Name the blood parasite species.
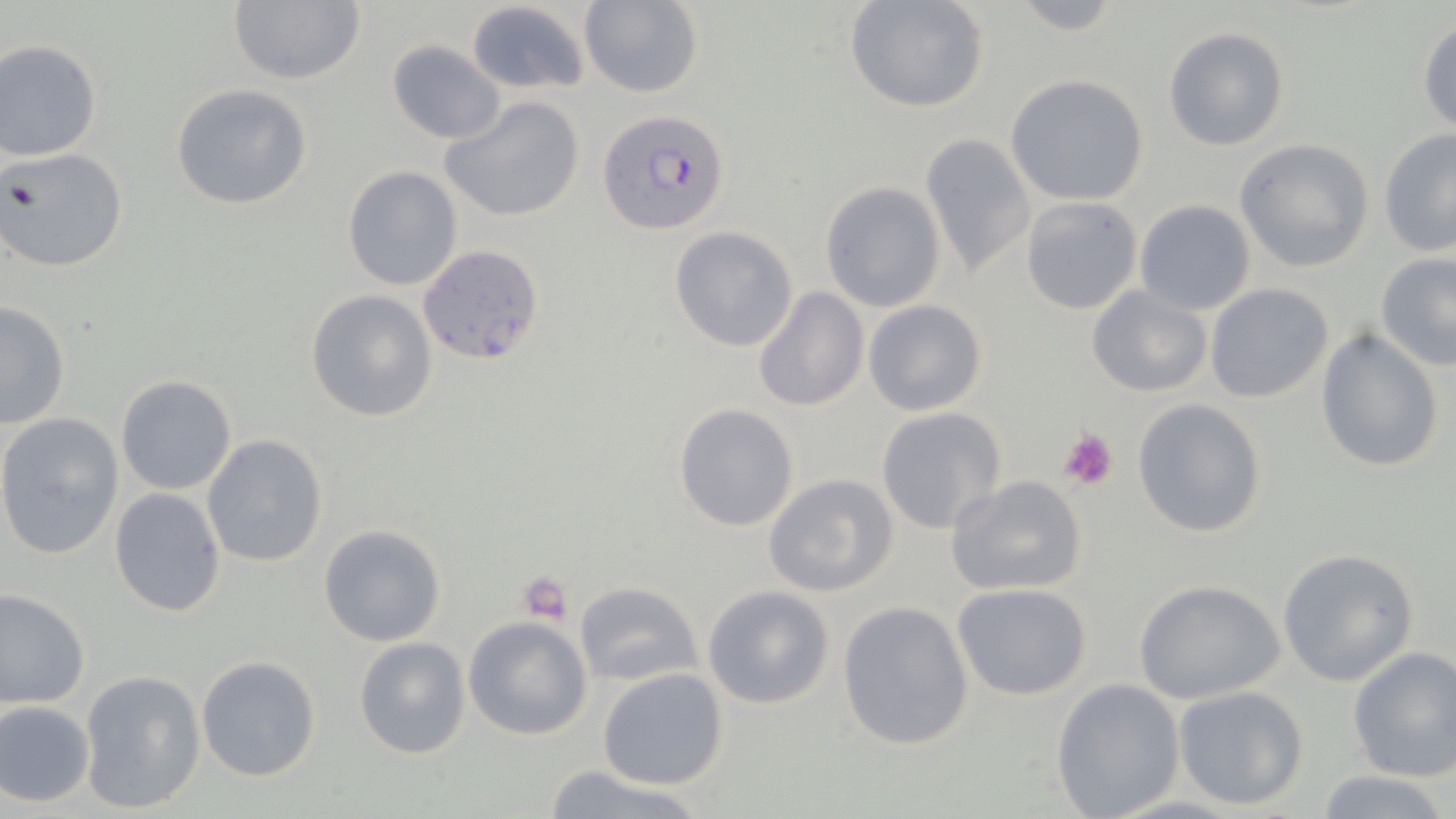
Plasmodium falciparum.

Approximate bounding boxes as (x1, y1, x2, y2) in pixels. Plasmodium falciparum-infected red blood cell locations: (597, 108, 731, 237). Uninfected red blood cell locations: (229, 0, 368, 86), (843, 0, 991, 115), (1002, 0, 1129, 36), (465, 1, 590, 94), (579, 1, 704, 98), (1418, 17, 1456, 133), (1162, 27, 1290, 152), (387, 38, 506, 145), (0, 39, 102, 162), (1005, 74, 1150, 206), (171, 83, 313, 210), (441, 95, 589, 223), (1379, 128, 1456, 258), (921, 133, 1034, 280), (1234, 138, 1374, 271), (0, 147, 128, 274), (341, 164, 463, 290), (819, 180, 946, 314), (1019, 196, 1142, 315), (1134, 199, 1256, 316), (668, 226, 800, 353), (418, 242, 545, 366), (1375, 253, 1456, 371), (1086, 283, 1212, 397), (1204, 284, 1333, 404), (751, 287, 869, 411), (305, 289, 438, 424), (863, 300, 988, 417), (0, 301, 71, 429), (1315, 328, 1443, 473), (114, 375, 237, 496), (1131, 398, 1268, 539), (673, 403, 799, 533), (874, 406, 1007, 536), (0, 412, 124, 560), (201, 434, 329, 568), (761, 473, 898, 597), (945, 475, 1088, 597), (109, 488, 228, 617), (319, 524, 448, 647), (1277, 548, 1421, 687), (1132, 578, 1286, 705), (574, 582, 699, 687), (952, 583, 1095, 701), (703, 585, 835, 710), (0, 588, 91, 709), (837, 601, 975, 750), (464, 615, 592, 739), (354, 636, 470, 759), (1347, 645, 1456, 781), (195, 654, 322, 783), (597, 668, 730, 789), (78, 669, 206, 814), (1051, 678, 1185, 818), (1173, 686, 1310, 811), (0, 699, 97, 808), (537, 764, 710, 819), (1312, 769, 1451, 819). Platelet locations: (1057, 427, 1119, 492), (518, 571, 574, 623). One field of a larger specimen. Captured at 1000x magnification. Optical microscopy. Image is 1456×819 pixels. May-Grünwald-Giemsa-stained preparation. Thin blood film.